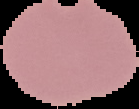
image_type: segmented cell region with the area outside set to black
preparation: thin blood film
malaria_status: uninfected
image_size: 139×109 pixels